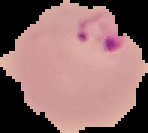 Image is 148×133 pixels. From a thin blood film. Segmented cell region on a black background. Malaria status: parasitized.